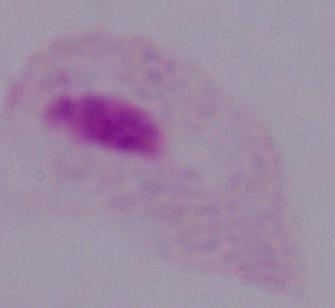

{
  "modality": "micrograph",
  "identification": "trichomonad",
  "magnification": "1000x"
}